Assess the morphology of the red blood cells.
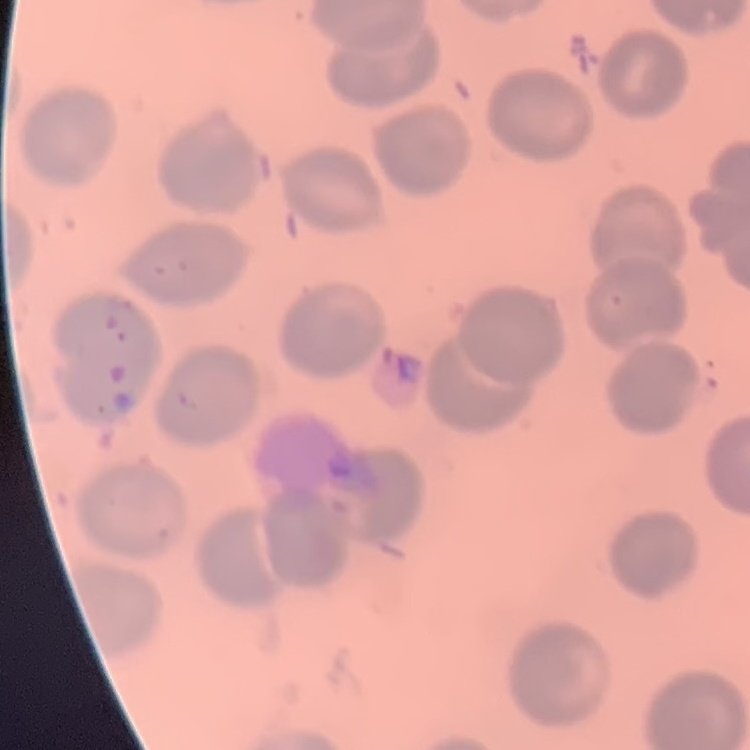
They show no rouleaux formation.

preparation: thin peripheral smear
image_type: one tile cut from a larger photomicrograph
stain: Field's or Giemsa